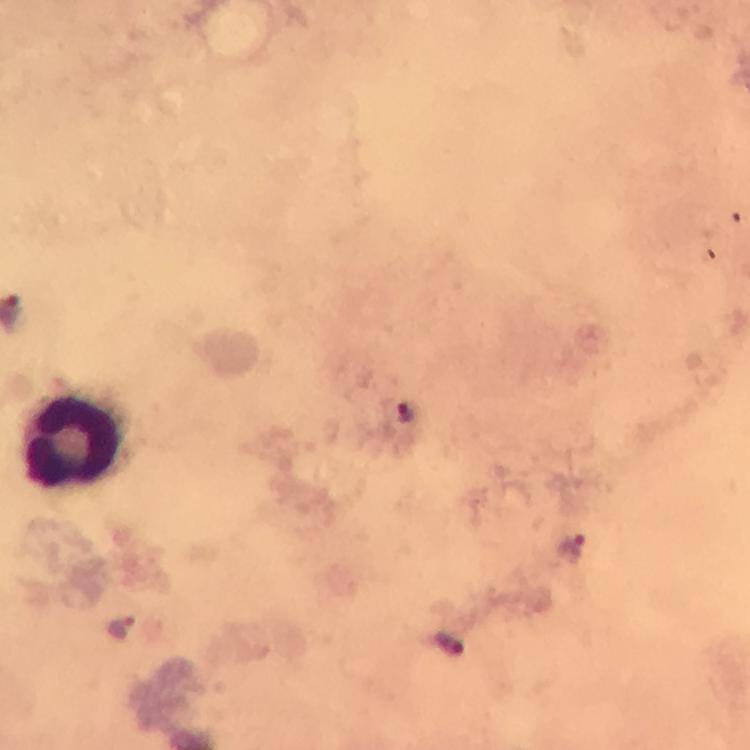
Approximate object centers, in pixels from the top-left corner. Malaria parasite locations: (x=405, y=412), (x=570, y=549), (x=122, y=626), (x=449, y=643). Leukocyte locations: (x=70, y=442). From a malaria diagnostic workup. Giemsa-stained preparation. Photographed with a smartphone mounted on the microscope. Immersion oil applied. Thick smear. Cropped region of a single field of view. Image is 750×750 pixels. 100x magnification.